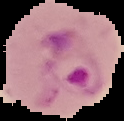

Summary:
  - Preparation: thin blood smear
  - Image size: 124×121 pixels
  - Image type: segmented cell region on a black background
  - Result: malaria parasites detected